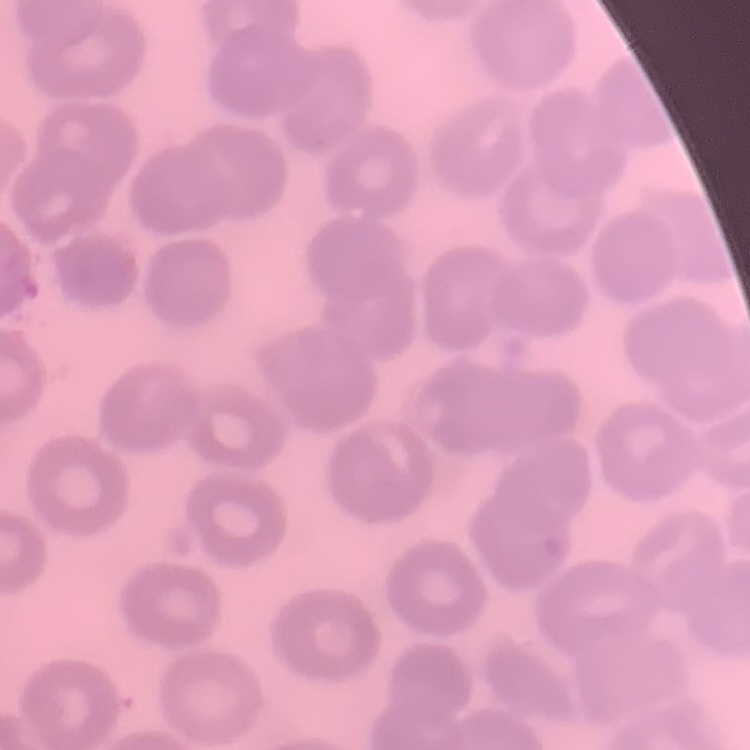 The red blood cells exhibit no rouleaux formation. Thin blood smear. Field's or Giemsa stain. Square crop of a larger photomicrograph.